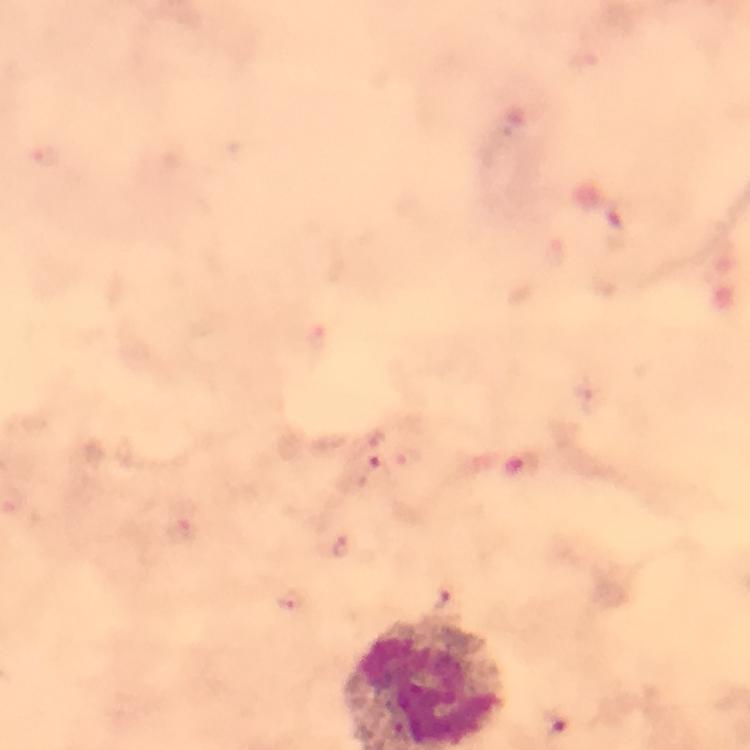

{
  "cropped_from": "one field of view",
  "image_size": "750×750 pixels",
  "magnification": "100x",
  "preparation": "thick blood smear",
  "immersion_oil": "used",
  "context": "from a malaria diagnostic workup",
  "capture": "smartphone camera through the microscope",
  "malaria_parasite_locations": "approximate centers as (x, y) in pixels: (378, 440), (341, 545), (289, 600), (555, 727)",
  "stain": "Giemsa"
}